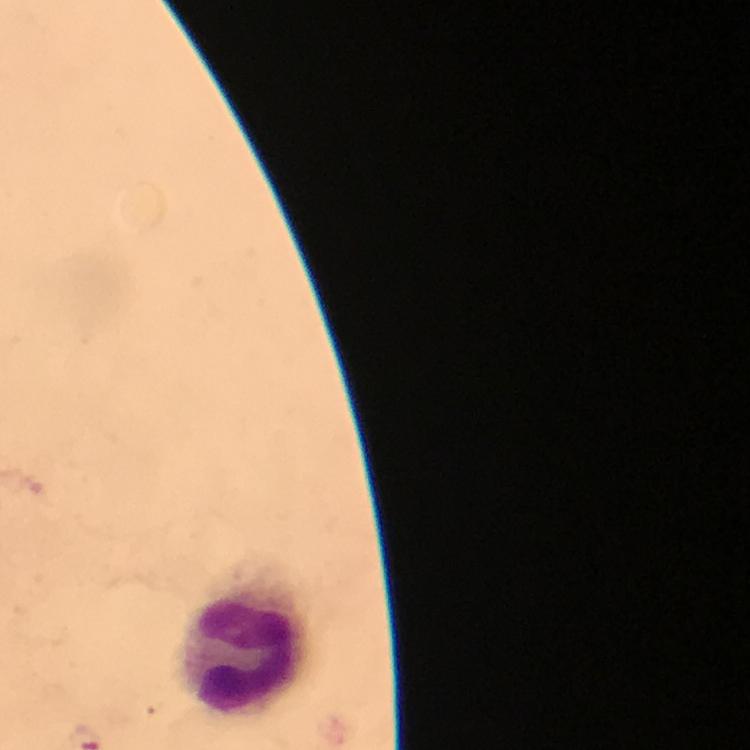
{
  "stain": "Giemsa",
  "image_size": "750×750 pixels",
  "cropped_from": "one field of view",
  "capture": "smartphone photograph through a microscope",
  "leukocyte_locations": "approximate centers as [x, y] in pixels: [245, 653]",
  "context": "from a malaria diagnostic workup",
  "immersion_oil": "used",
  "preparation": "thick blood smear",
  "plasmodium_parasites": "none seen",
  "magnification": "100x"
}